Identify the cell.
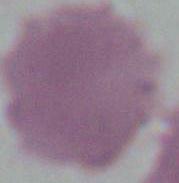
An erythrocyte.

magnification = 1000x
modality = micrograph